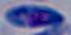

{
  "modality": "micrograph",
  "magnification": "1000x",
  "identification": "Toxoplasma gondii"
}